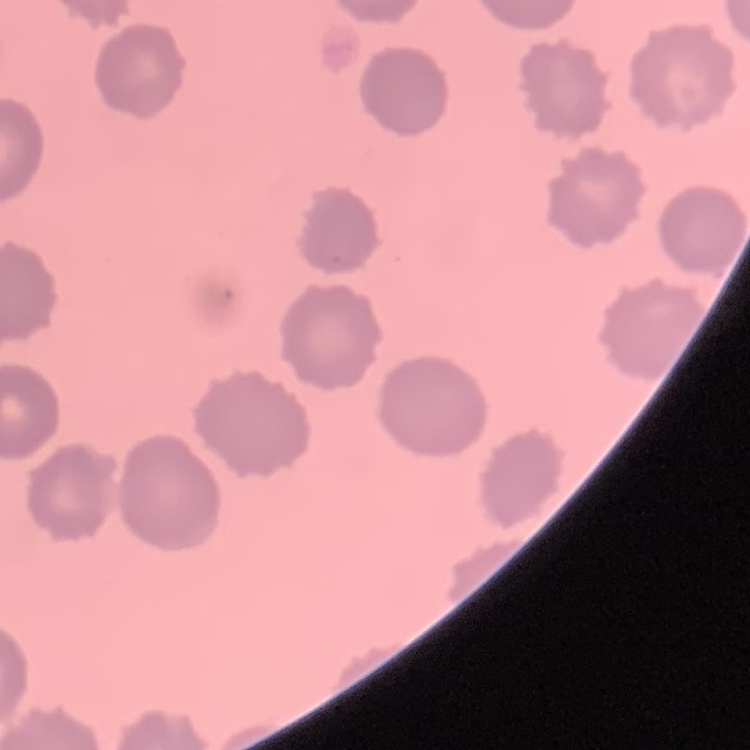
red blood cell morphology = no rouleaux formation
image type = square crop of a larger photomicrograph
preparation = thin peripheral smear
stain = Field's or Giemsa